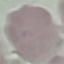

{
  "result": "negative for malaria parasites",
  "capture": "smartphone camera at the microscope eyepiece",
  "stain": "Giemsa",
  "preparation": "thin blood film",
  "image_type": "automatically extracted cell patch, resized to 64 × 64 pixels"
}